Locate and identify every blood parasite.
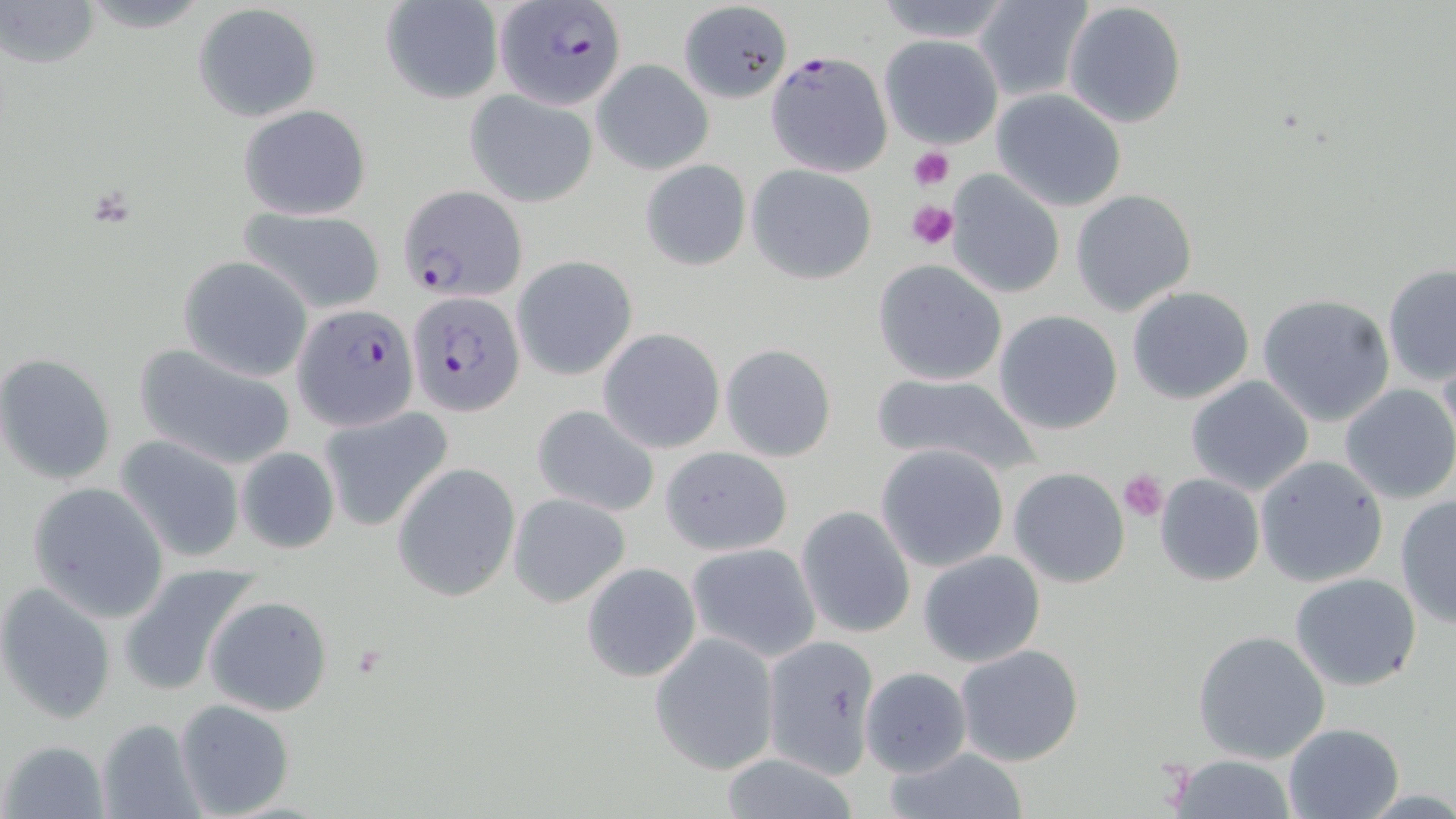
Approximate bounding boxes as named x1/y1/x2/y2 corners in pixels.
Plasmodium falciparum-infected red blood cells: (x1=493, y1=1, x2=629, y2=110), (x1=765, y1=51, x2=894, y2=177), (x1=398, y1=183, x2=527, y2=302), (x1=407, y1=291, x2=525, y2=418), (x1=295, y1=302, x2=421, y2=431).
No Plasmodium ovale, Plasmodium malariae, Plasmodium vivax, Babesia divergens, or Trypanosoma brucei observed.

Uninfected red blood cell locations: (x1=3, y1=0, x2=101, y2=70), (x1=871, y1=0, x2=1016, y2=44), (x1=973, y1=0, x2=1093, y2=100), (x1=378, y1=1, x2=504, y2=105), (x1=1062, y1=2, x2=1188, y2=129), (x1=193, y1=3, x2=321, y2=122), (x1=678, y1=4, x2=792, y2=106), (x1=878, y1=34, x2=1005, y2=150), (x1=592, y1=59, x2=712, y2=175), (x1=992, y1=88, x2=1128, y2=211), (x1=465, y1=89, x2=599, y2=206), (x1=238, y1=103, x2=373, y2=220), (x1=640, y1=159, x2=753, y2=271), (x1=746, y1=164, x2=877, y2=284), (x1=944, y1=170, x2=1067, y2=298), (x1=1070, y1=189, x2=1198, y2=315), (x1=239, y1=208, x2=387, y2=314), (x1=511, y1=256, x2=638, y2=381), (x1=178, y1=257, x2=311, y2=382), (x1=872, y1=259, x2=1008, y2=386), (x1=1381, y1=263, x2=1456, y2=388), (x1=1127, y1=286, x2=1254, y2=404), (x1=1258, y1=294, x2=1396, y2=428), (x1=993, y1=309, x2=1124, y2=435), (x1=598, y1=328, x2=726, y2=452), (x1=132, y1=342, x2=298, y2=470), (x1=721, y1=343, x2=837, y2=461), (x1=0, y1=351, x2=118, y2=486), (x1=866, y1=373, x2=1044, y2=481), (x1=1186, y1=375, x2=1313, y2=496), (x1=1339, y1=385, x2=1456, y2=504), (x1=532, y1=404, x2=660, y2=518), (x1=318, y1=405, x2=455, y2=533), (x1=115, y1=436, x2=247, y2=564), (x1=875, y1=443, x2=1010, y2=572), (x1=235, y1=446, x2=340, y2=555), (x1=660, y1=447, x2=792, y2=557), (x1=1254, y1=455, x2=1389, y2=587), (x1=391, y1=463, x2=521, y2=601), (x1=1008, y1=467, x2=1130, y2=588), (x1=1155, y1=473, x2=1264, y2=586), (x1=27, y1=482, x2=170, y2=622), (x1=507, y1=491, x2=632, y2=608), (x1=1394, y1=495, x2=1456, y2=628), (x1=795, y1=504, x2=915, y2=639), (x1=685, y1=543, x2=821, y2=662), (x1=918, y1=550, x2=1045, y2=667), (x1=580, y1=563, x2=701, y2=683), (x1=115, y1=566, x2=261, y2=696), (x1=1289, y1=572, x2=1422, y2=692), (x1=1, y1=583, x2=118, y2=724), (x1=205, y1=596, x2=333, y2=716), (x1=1192, y1=631, x2=1331, y2=763), (x1=650, y1=632, x2=780, y2=774), (x1=763, y1=635, x2=879, y2=775), (x1=954, y1=644, x2=1086, y2=767), (x1=859, y1=668, x2=971, y2=777), (x1=176, y1=698, x2=296, y2=816), (x1=96, y1=717, x2=206, y2=819), (x1=1280, y1=721, x2=1404, y2=819), (x1=3, y1=738, x2=108, y2=817), (x1=884, y1=746, x2=1030, y2=819), (x1=1167, y1=753, x2=1298, y2=817), (x1=713, y1=755, x2=870, y2=818). Platelet locations: (x1=909, y1=147, x2=953, y2=191), (x1=907, y1=200, x2=960, y2=248), (x1=1118, y1=470, x2=1167, y2=522). Slide-level diagnosis: Plasmodium falciparum. Image is 1456×819 pixels. Thin blood film. May-Grünwald-Giemsa-stained preparation. One field of a larger specimen. Optical microscopy. 1000x magnification.